Locate every blood parasite and identify its species.
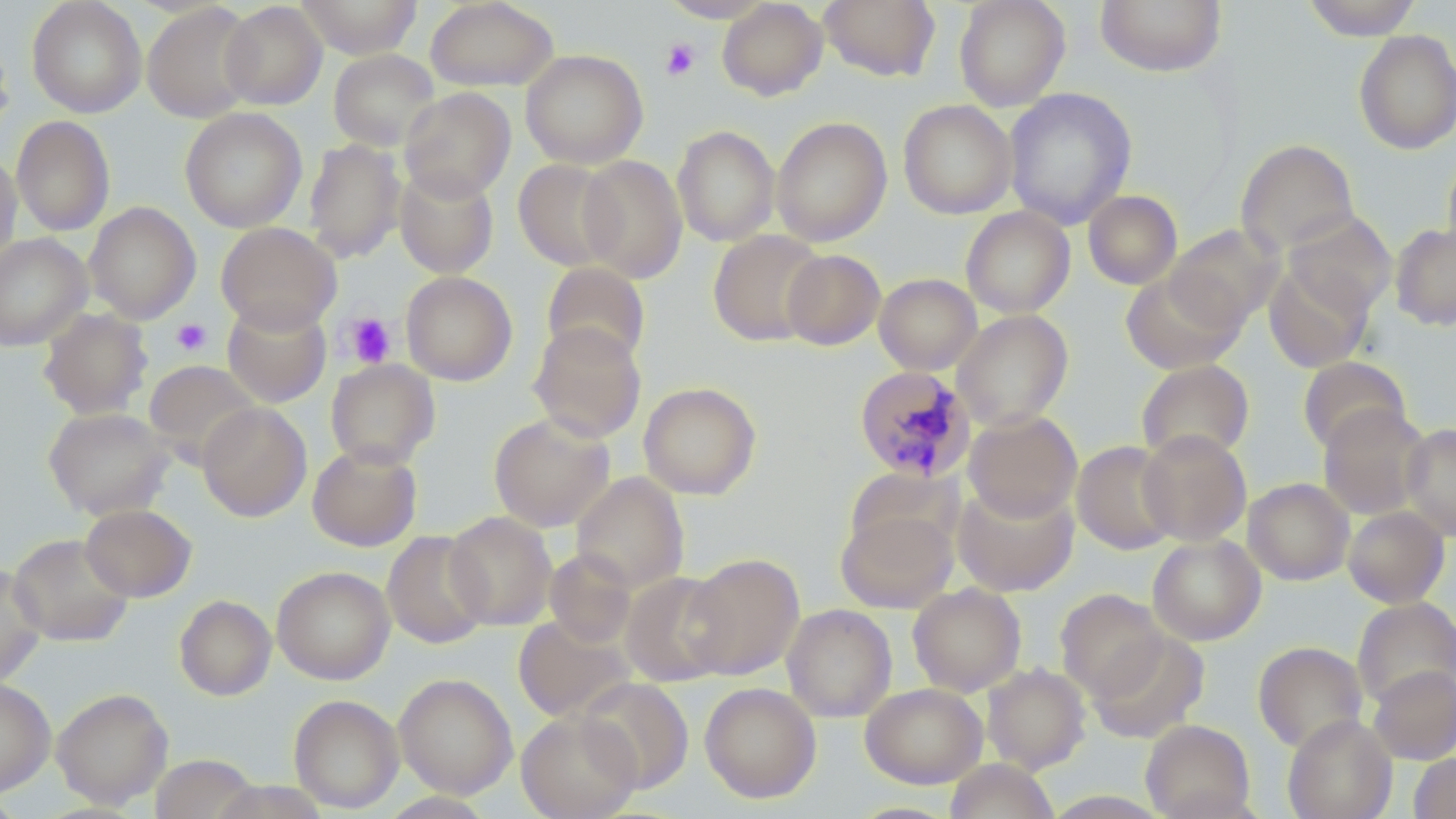

Approximate bounding boxes as [x1, y1, x2, y2] in pixels.
Plasmodium malariae-infected red blood cells: [854, 365, 975, 482].
No Plasmodium falciparum, Plasmodium ovale, Plasmodium vivax, Babesia divergens, or Trypanosoma brucei observed.

Platelet locations: [661, 38, 700, 80], [343, 312, 397, 369], [171, 318, 212, 356]. Uninfected red blood cell locations: [26, 0, 147, 118], [296, 0, 422, 59], [425, 0, 558, 92], [658, 0, 774, 22], [717, 0, 828, 101], [820, 0, 940, 82], [953, 0, 1071, 111], [1096, 0, 1226, 76], [1301, 0, 1422, 40], [219, 2, 327, 110], [142, 3, 259, 123], [1353, 29, 1456, 155], [0, 32, 14, 140], [328, 49, 440, 152], [521, 49, 648, 169], [399, 87, 516, 201], [1003, 87, 1137, 229], [898, 99, 1017, 219], [180, 107, 307, 233], [11, 115, 115, 236], [771, 116, 892, 247], [672, 125, 781, 246], [303, 139, 406, 262], [1236, 139, 1359, 256], [1442, 150, 1456, 262], [0, 151, 22, 265], [577, 154, 688, 283], [513, 159, 622, 271], [394, 166, 499, 278], [1083, 190, 1183, 289], [83, 202, 201, 324], [960, 206, 1075, 318], [1283, 210, 1397, 317], [216, 222, 342, 333], [1390, 223, 1456, 331], [1165, 224, 1283, 330], [708, 229, 826, 346], [0, 233, 93, 351], [781, 248, 886, 350], [1264, 261, 1374, 372], [542, 262, 651, 368], [1120, 270, 1244, 374], [401, 271, 518, 386], [874, 274, 981, 375], [222, 301, 331, 407], [39, 307, 153, 420], [952, 310, 1073, 429], [529, 322, 646, 442], [1297, 356, 1411, 455], [326, 359, 440, 469], [1136, 359, 1254, 465], [144, 360, 262, 465], [639, 382, 762, 500], [196, 402, 312, 522], [1318, 403, 1430, 519], [43, 407, 175, 520], [964, 410, 1082, 522], [489, 412, 615, 532], [1400, 422, 1456, 541], [1138, 429, 1252, 546], [1072, 441, 1180, 555], [307, 443, 422, 551], [844, 469, 960, 557], [571, 472, 689, 593], [1243, 478, 1354, 585], [952, 482, 1079, 596], [80, 503, 196, 602], [836, 505, 959, 613], [1343, 506, 1450, 607], [444, 511, 557, 630], [382, 530, 492, 649], [8, 533, 134, 646], [1148, 534, 1265, 645], [545, 549, 637, 647], [683, 552, 804, 679], [0, 563, 45, 686], [272, 566, 395, 684], [619, 571, 734, 686], [908, 583, 1026, 696], [1055, 589, 1167, 700], [174, 595, 276, 701], [1352, 597, 1456, 709], [783, 604, 897, 722], [513, 615, 635, 722], [1088, 631, 1208, 742], [1253, 640, 1367, 753], [982, 663, 1090, 774], [1368, 665, 1456, 765], [394, 673, 518, 798], [576, 677, 694, 794], [0, 678, 55, 796], [699, 682, 821, 803], [860, 682, 987, 788], [51, 688, 173, 807], [289, 694, 404, 813], [516, 710, 642, 819], [1283, 714, 1396, 819], [1140, 719, 1255, 819], [1409, 753, 1456, 819], [150, 754, 259, 819], [944, 759, 1057, 819]. Slide-level diagnosis: Plasmodium malariae. Optical microscopy. May-Grünwald-Giemsa-stained preparation. Image is 1456×819 pixels. Thin blood film. One field of a larger specimen. 1000x magnification.